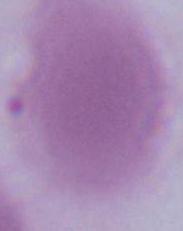
Summary:
  - Modality: photomicrograph
  - Magnification: 1000x
  - Identification: erythrocyte